Assess the morphology of the erythrocytes.
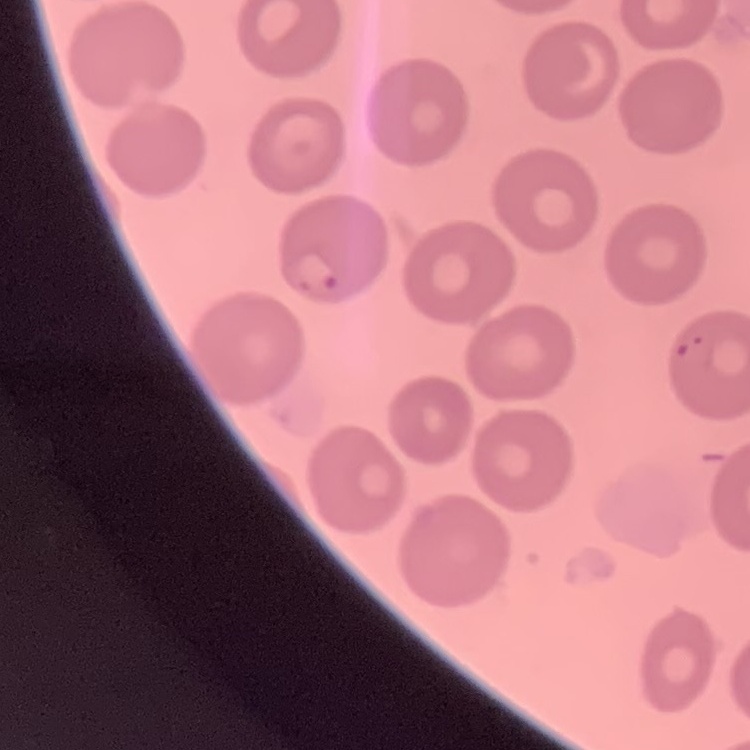

They show no rouleaux formation.

Thin blood film. Field's or Giemsa stain. Square crop of a larger photomicrograph.